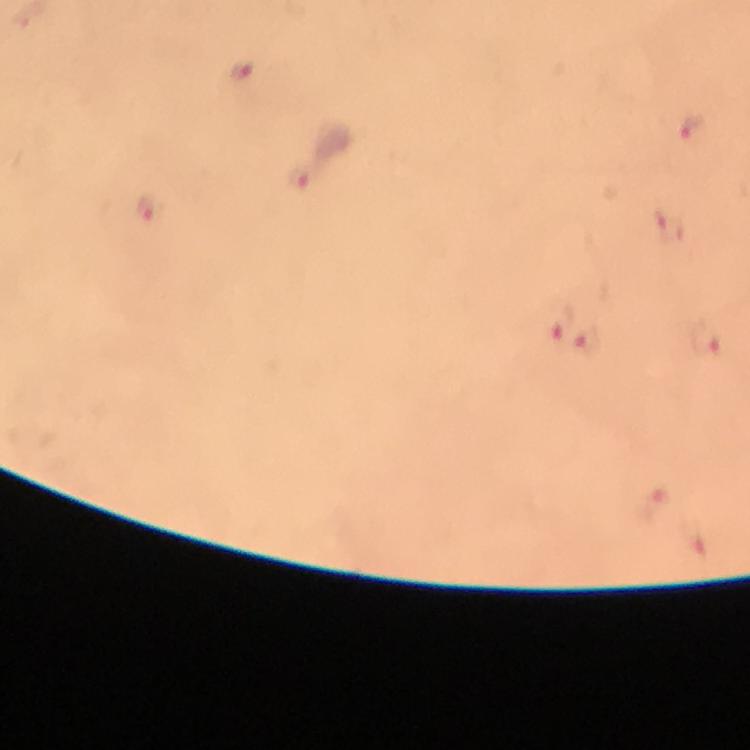
Approximate centers as [x, y] in pixels.
Summary:
  - Plasmodium parasite locations: [241, 71], [692, 127], [299, 179], [146, 208], [671, 228], [556, 322], [708, 340], [587, 341], [650, 504], [695, 544]
  - Stain: Giemsa
  - Preparation: thick blood smear
  - Context: from a diagnostic examination for malaria
  - Cropped from: one field of view
  - Image size: 750×750 pixels
  - Immersion oil: applied
  - Capture: smartphone camera through the microscope
  - Magnification: 100x